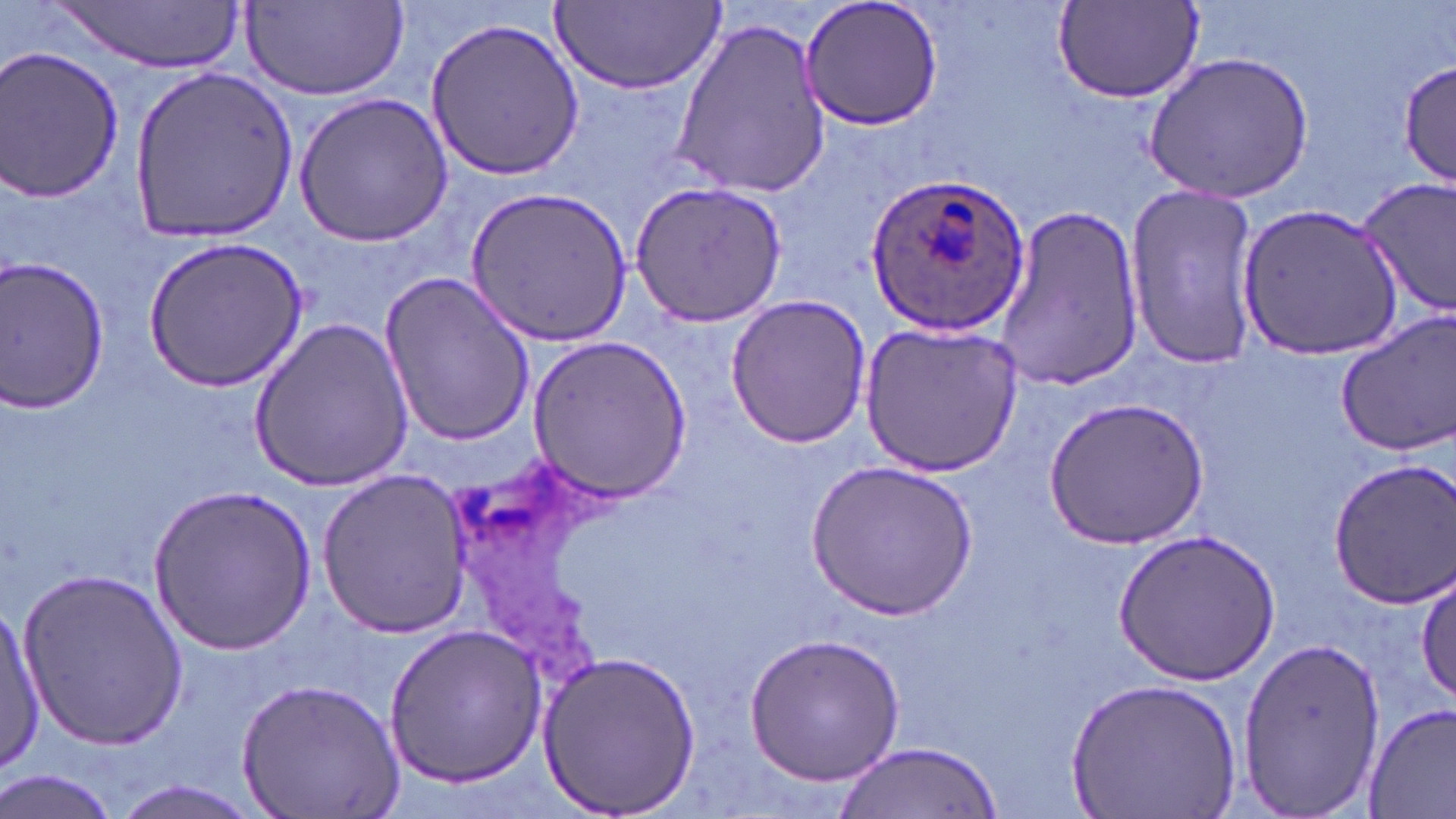
Summary:
  - Coordinate format: approximate bounding boxes as (x1, y1, x2, y2) in pixels
  - Uninfected red blood cell locations: (798, 0, 946, 133), (55, 1, 245, 74), (243, 1, 409, 104), (549, 1, 724, 93), (1053, 2, 1208, 107), (423, 16, 585, 180), (669, 17, 833, 198), (0, 44, 125, 205), (1143, 54, 1314, 204), (1399, 57, 1453, 192), (126, 66, 303, 241), (293, 91, 453, 246), (1357, 178, 1456, 318), (629, 179, 787, 327), (1122, 183, 1260, 373), (469, 185, 633, 347), (1238, 197, 1403, 359), (989, 201, 1143, 392), (144, 236, 308, 390), (0, 256, 110, 415), (378, 270, 535, 449), (724, 295, 874, 449), (1336, 311, 1456, 457), (249, 314, 415, 490), (858, 321, 1027, 479), (526, 334, 696, 502), (1043, 396, 1209, 551), (1327, 455, 1456, 608), (808, 460, 977, 621), (316, 469, 476, 639), (149, 484, 316, 654), (1110, 527, 1280, 686), (1414, 567, 1456, 708), (16, 569, 194, 747), (1, 603, 44, 777), (381, 621, 546, 788), (742, 632, 907, 786), (1236, 638, 1387, 813), (538, 650, 703, 816), (235, 674, 404, 819), (1065, 675, 1244, 819), (1362, 703, 1456, 817), (833, 740, 1000, 818), (1, 768, 122, 819), (111, 777, 264, 819)
  - Plasmodium ovale-infected red blood cell locations: (863, 170, 1033, 339)
  - Slide-level diagnosis: Plasmodium ovale
  - Magnification: 1000x
  - Preparation: thin blood smear
  - Modality: light microscopy
  - Stain: May-Grünwald-Giemsa
  - Image size: 1456×819 pixels
  - Field of view: single